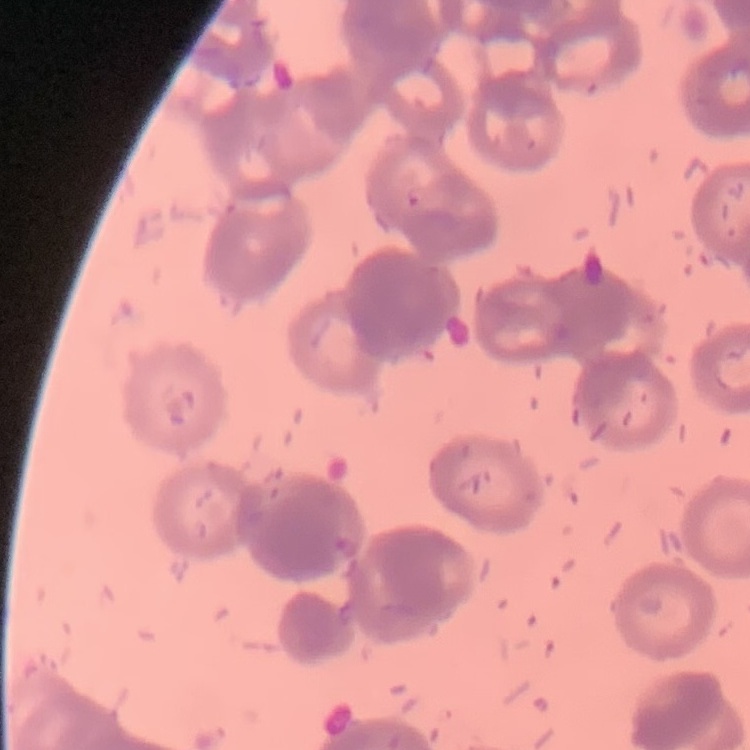

{
  "erythrocyte_morphology": "rouleaux formation",
  "image_type": "square crop of a larger photomicrograph",
  "stain": "Field's or Giemsa",
  "preparation": "thin peripheral smear"
}